Identify the preparation type.
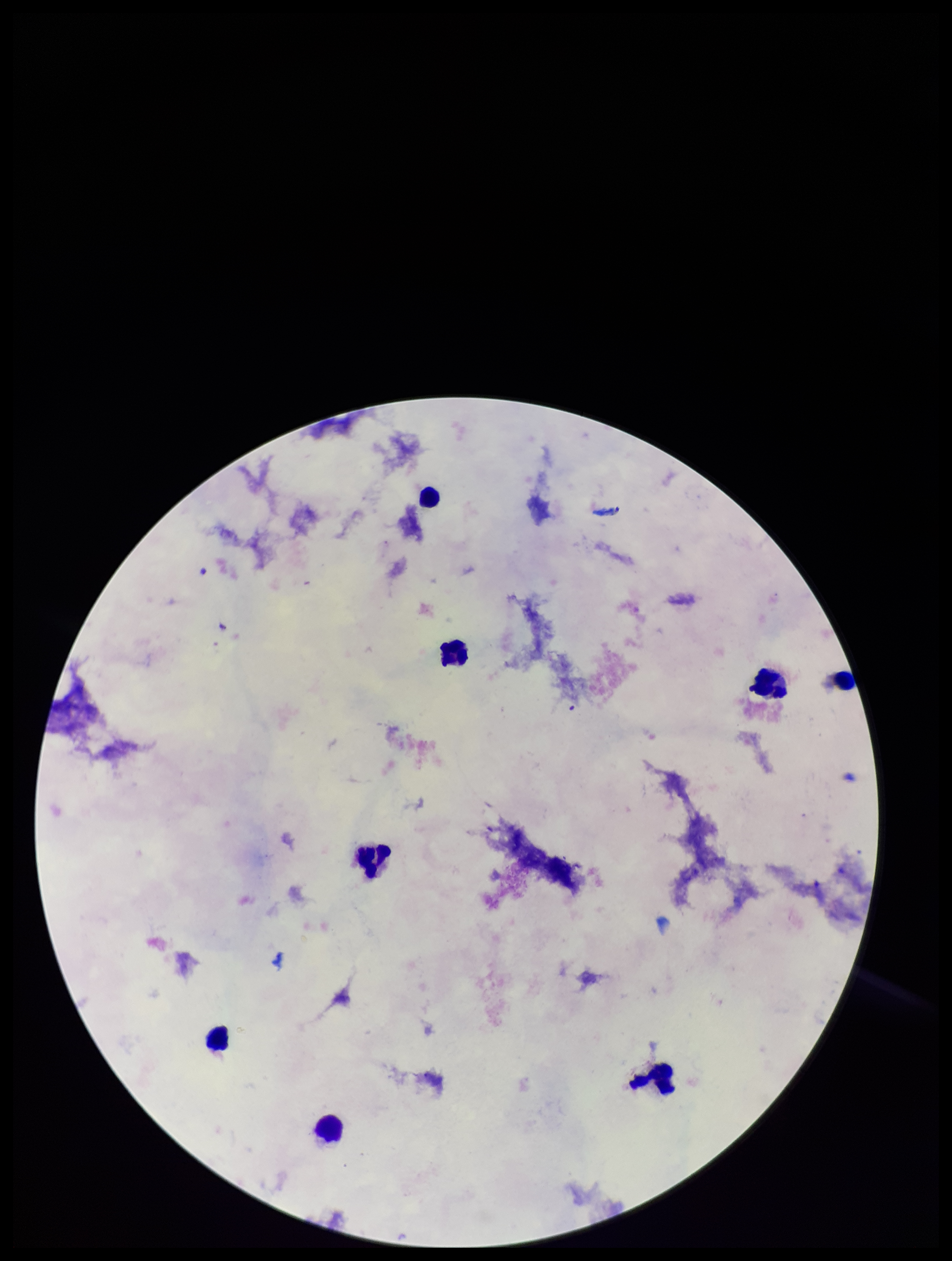

A thick smear.

patient_malaria_status: negative
field_of_view: single
image_size: 952×1261 pixels
parasite_count: 0
capture: smartphone photograph through the microscope eyepiece
stain: Giemsa
plasmodium_parasites: none detected
leukocyte_count: 8